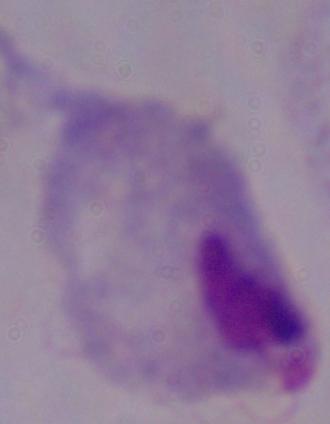

{
  "identification": "trichomonad",
  "magnification": "1000x",
  "modality": "micrograph"
}